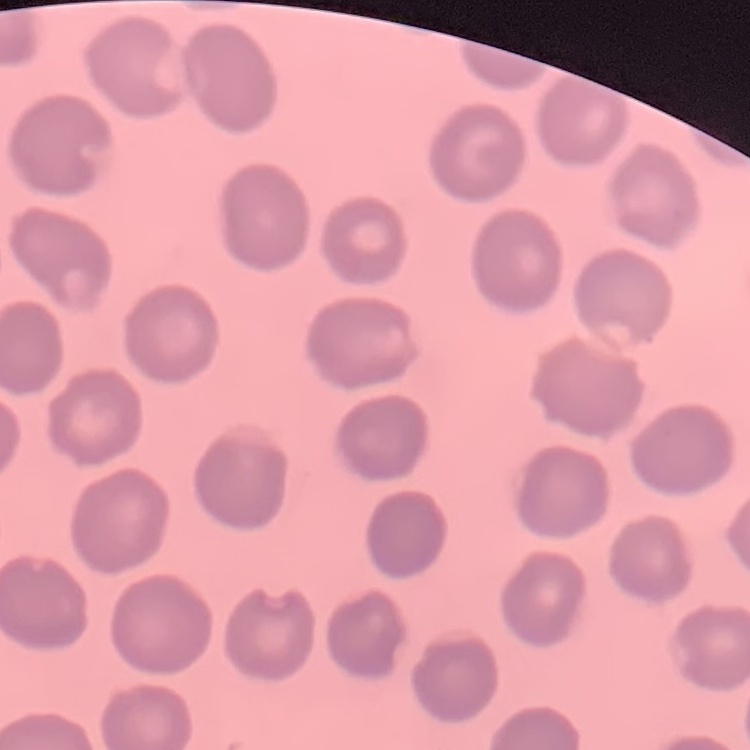

erythrocyte morphology = no rouleaux formation
stain = Field's or Giemsa
image type = one tile cut from a larger photomicrograph
preparation = thin blood film